Identify the cell.
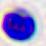

A leukocyte.

Summary:
  - Modality: photomicrograph
  - Magnification: 400x